Report the malaria status of this cell.
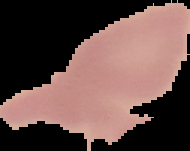

Uninfected.

Image is 190×151 pixels. From a thin blood film. The area outside the segmented cell region is set to black.